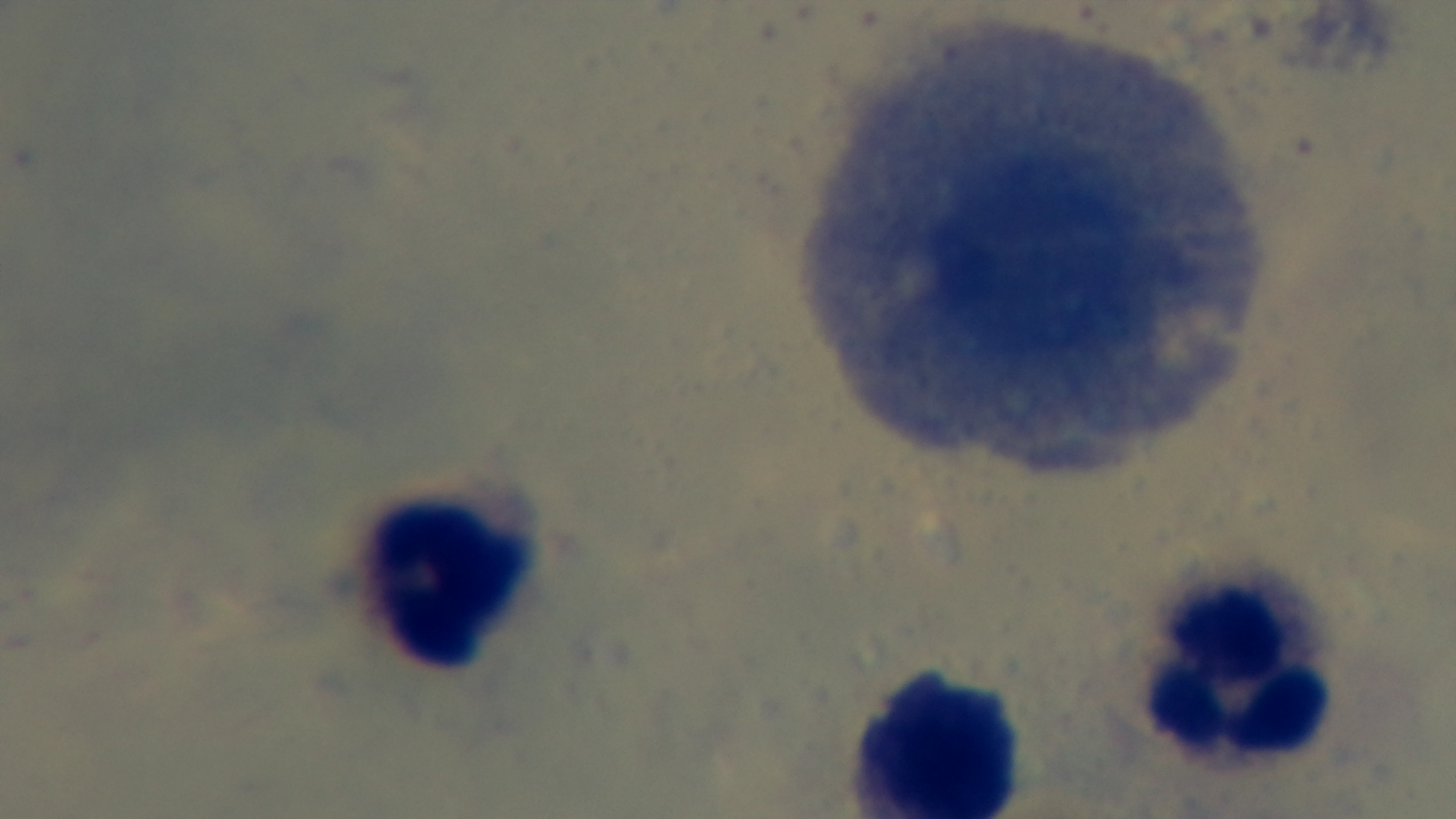
preparation = thick blood film
stain = Giemsa
capture = mounted 4K digital camera
malaria status = negative
modality = light microscopy
objective = 100x oil immersion
field of view = single